Classify this cell by malaria status.
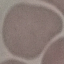

It is uninfected.

Summary:
  - Preparation: thin blood smear
  - Stain: Giemsa
  - Capture: smartphone camera at the microscope eyepiece
  - Image type: automatically extracted cell patch, resized to 64 × 64 pixels